Look for Plasmodium parasites.
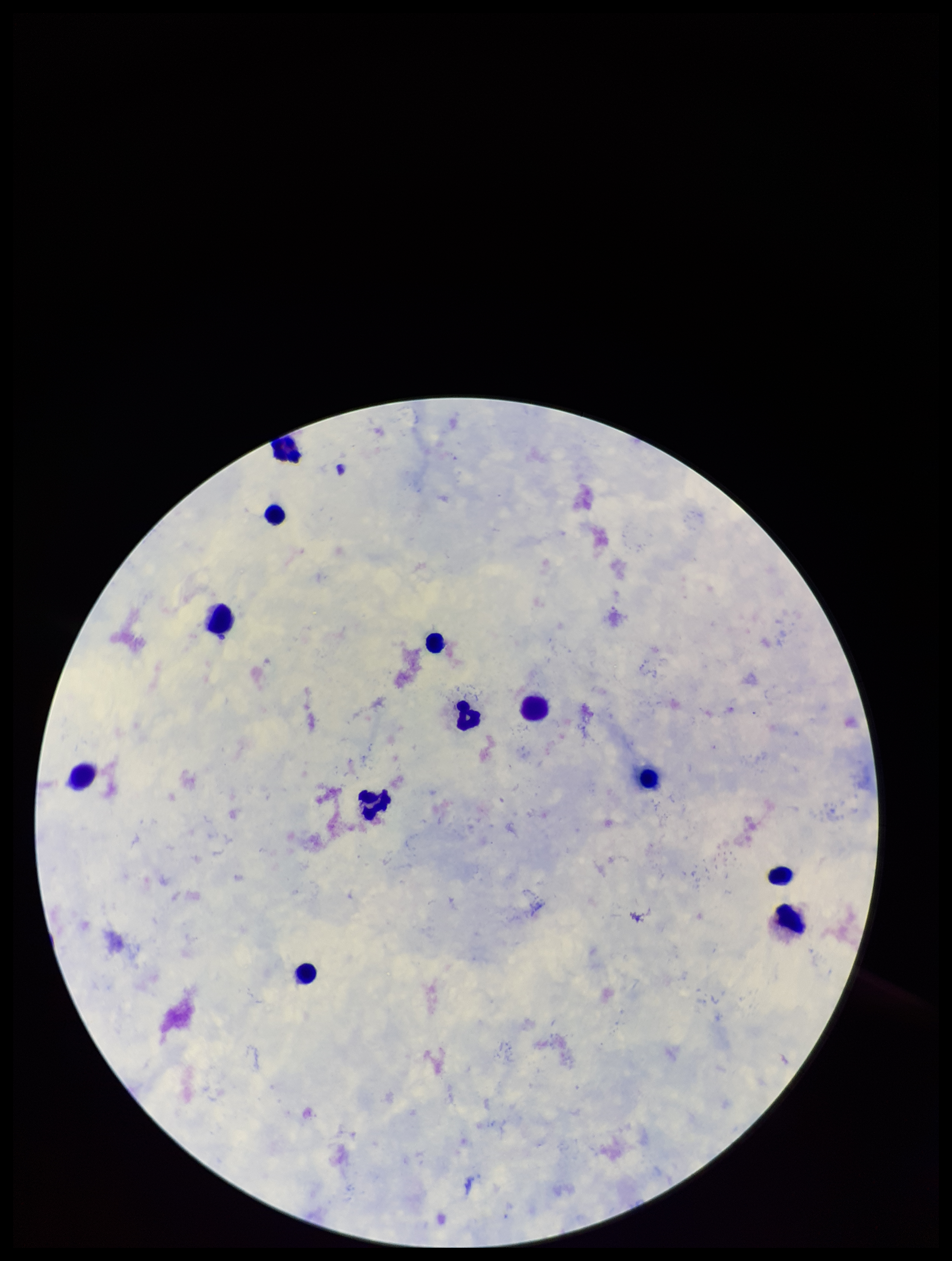

None detected.

Leukocyte count: 12. Smartphone photograph taken through the eyepiece of a microscope. Stained with Giemsa. Patient malaria status: negative. Image is 952×1261 pixels. One field from this slide. Parasite count: 0. Preparation: thick smear.